Classify this cell by malaria status.
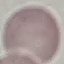
It is uninfected.

Acquired by smartphone through the microscope eyepiece. Thin blood film. Giemsa-stained preparation. Cell patch, automatically extracted from a larger field of view and resized to 64 × 64 pixels.